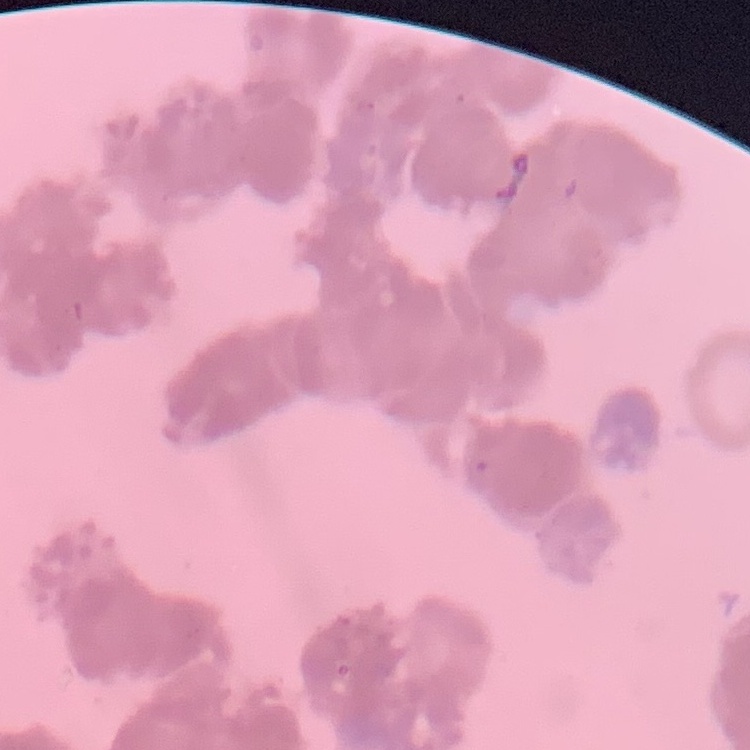
{
  "red_blood_cell_morphology": "rouleaux formation",
  "image_type": "square crop of a larger photomicrograph",
  "preparation": "thin peripheral smear",
  "stain": "Field's or Giemsa"
}